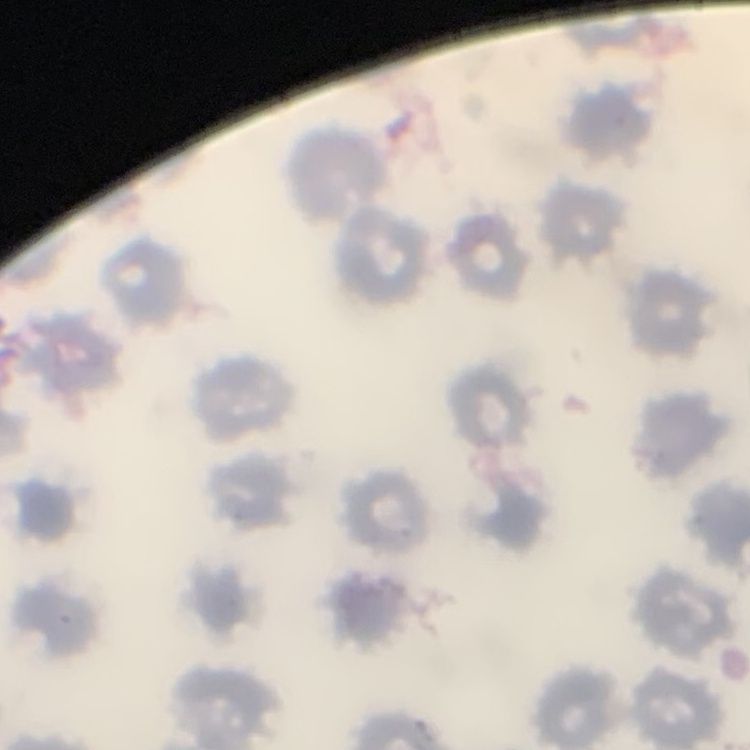
Summary:
  - Erythrocyte morphology: no rouleaux formation
  - Preparation: thin blood film
  - Image type: square crop of a larger photomicrograph
  - Stain: Field's or Giemsa